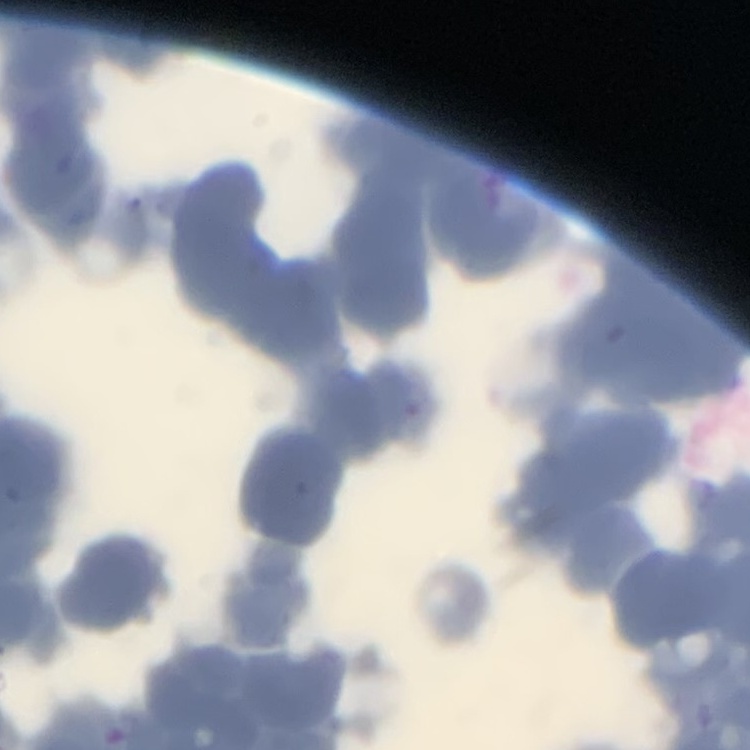
Summary:
  - Erythrocyte morphology: rouleaux formation
  - Preparation: thin blood smear
  - Image type: one tile cut from a larger photomicrograph
  - Stain: Field's or Giemsa